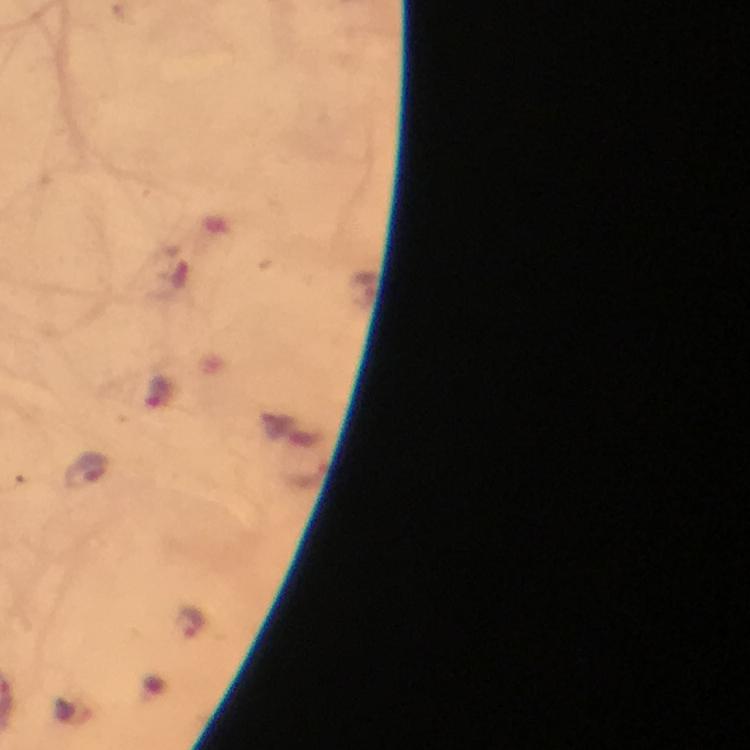
Approximate object centers, in pixels from the top-left corner. Malaria parasite locations: (x=190, y=621). Giemsa stain. From a malaria diagnostic workup. Thick blood film. Image is 750×750 pixels. Photographed through the microscope with a smartphone camera. 100x magnification. Immersion oil was used. Cropped region of a single field of view.